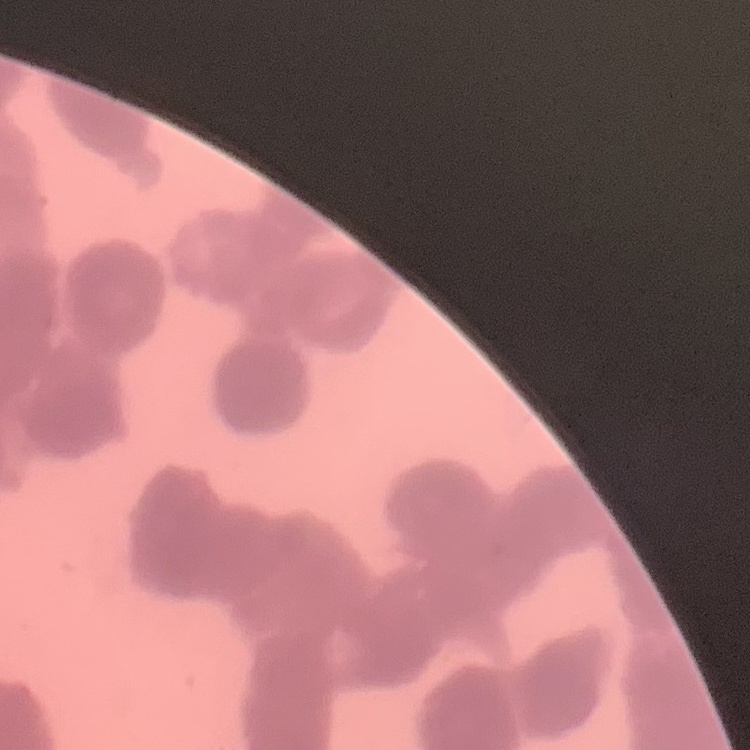
{
  "erythrocyte_morphology": "rouleaux formation",
  "stain": "Field's or Giemsa",
  "preparation": "thin blood smear",
  "image_type": "square crop of a larger photomicrograph"
}